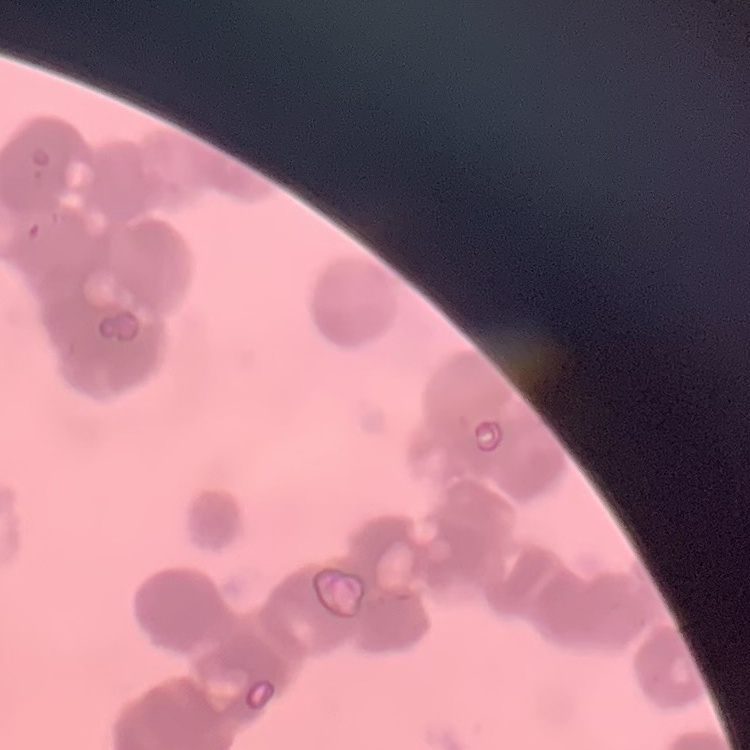
erythrocyte morphology = rouleaux formation
image type = square crop of a larger photomicrograph
preparation = thin blood film
stain = Field's or Giemsa